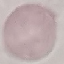

result = no malaria parasites detected
image type = automatically extracted cell patch, resized to 64 × 64 pixels
preparation = thin blood smear
capture = smartphone through the microscope eyepiece
stain = Giemsa